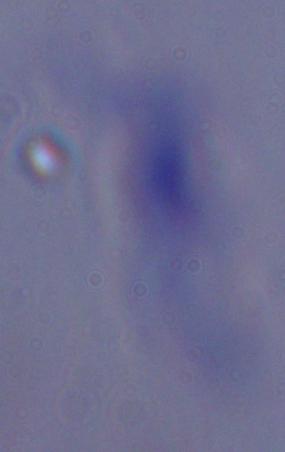
A trypanosome is shown. 1000x magnification. Photomicrograph.